Outline each blood parasite and name the species.
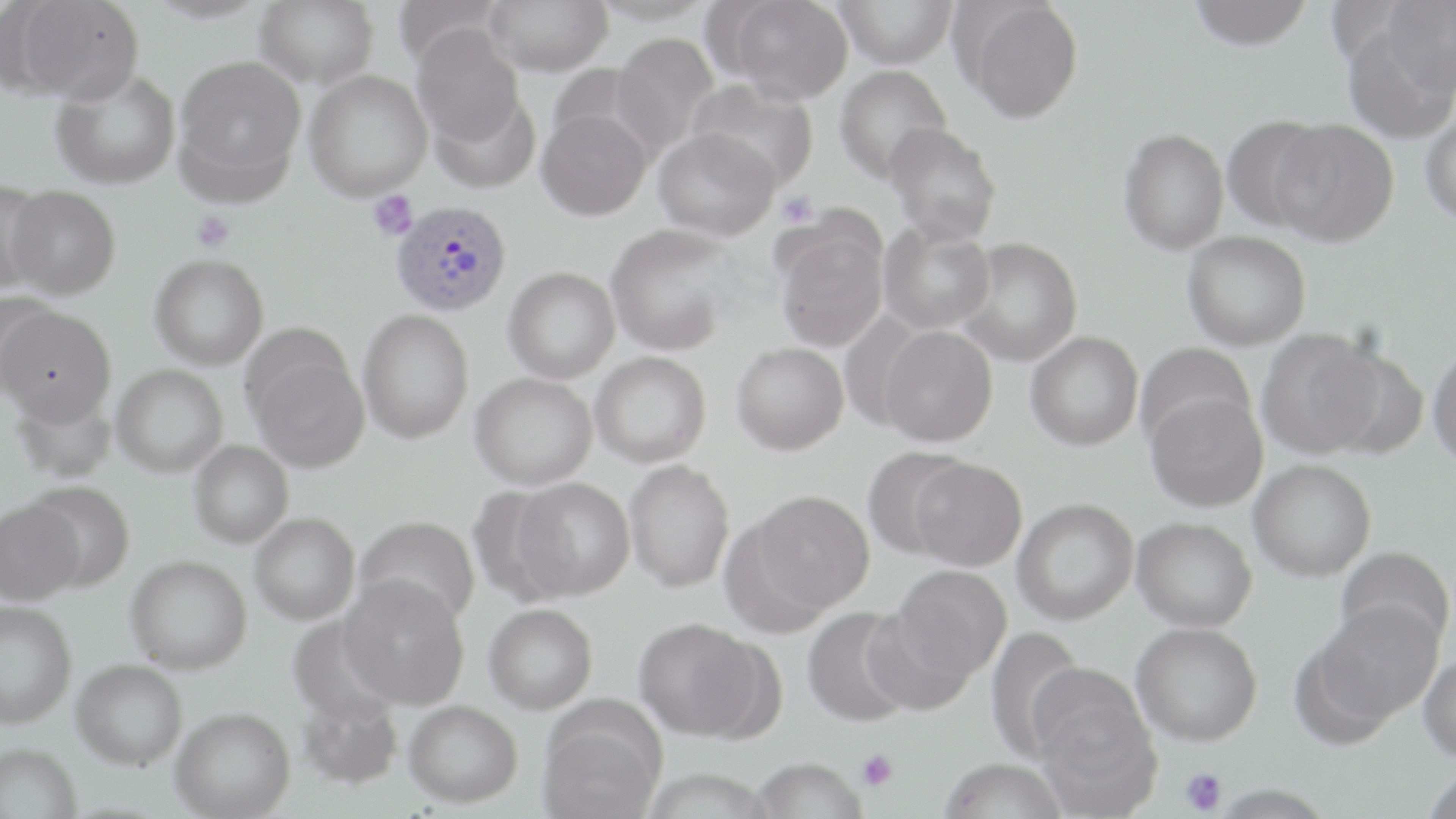
Approximate bounding boxes as (x1,y1)-(x2,y2) corner pairs in pixels.
Plasmodium vivax-infected red blood cells: (390,199)-(512,317).
No Plasmodium falciparum, Plasmodium ovale, Plasmodium malariae, Babesia divergens, or Trypanosoma brucei observed.

slide-level diagnosis = Plasmodium vivax
stain = May-Grünwald-Giemsa
preparation = thin blood smear
modality = light microscopy
uninfected red blood cell locations = approximate bounding boxes as (x1,y1)-(x2,y2) corner pairs in pixels: (11,0)-(144,103), (255,0)-(379,90), (485,0)-(613,76), (589,0)-(715,26), (725,0)-(853,104), (1187,0)-(1315,50), (1379,0)-(1456,102), (832,1)-(958,69), (961,2)-(1084,123), (411,25)-(526,148), (1342,26)-(1454,145), (611,32)-(719,156), (174,54)-(306,192), (834,64)-(952,184), (50,68)-(181,190), (303,68)-(432,201), (687,79)-(819,191), (425,90)-(539,194), (537,109)-(651,221), (1420,109)-(1456,225), (1220,115)-(1331,233), (1269,119)-(1399,246), (884,123)-(1002,245), (653,128)-(780,242), (1118,128)-(1229,255), (0,178)-(53,295), (6,184)-(121,299), (878,221)-(996,334), (605,224)-(738,356), (775,229)-(887,353), (1183,231)-(1311,350), (956,238)-(1083,366), (149,253)-(269,370), (503,266)-(620,383), (0,289)-(59,393), (0,305)-(115,425), (358,308)-(473,444), (879,325)-(998,447), (1256,330)-(1383,460), (1025,331)-(1143,451), (731,342)-(848,455), (1135,343)-(1255,451), (1428,344)-(1456,470), (1316,345)-(1430,459), (247,346)-(369,473), (590,351)-(711,468), (111,364)-(228,477), (470,372)-(597,491), (1145,392)-(1268,512), (188,440)-(293,548), (862,446)-(972,559), (909,457)-(1028,571), (1248,458)-(1376,582), (624,459)-(735,592), (513,478)-(635,600), (24,481)-(135,592), (752,489)-(874,612), (1013,498)-(1139,625), (0,499)-(85,606), (249,512)-(360,625), (354,515)-(480,628), (1132,516)-(1257,632), (1335,546)-(1455,652), (125,554)-(252,674), (892,564)-(1012,680), (339,575)-(470,709), (1311,599)-(1445,728), (0,600)-(78,728), (484,603)-(597,714), (801,607)-(917,727), (861,607)-(976,716), (633,618)-(765,740), (1131,622)-(1262,746), (982,625)-(1087,761), (1418,653)-(1456,763), (71,658)-(187,770), (296,693)-(403,791), (1031,694)-(1162,819), (403,700)-(523,807), (170,706)-(295,818), (538,717)-(664,819), (0,742)-(83,819), (751,757)-(867,819), (938,758)-(1068,819), (1420,765)-(1456,819), (640,768)-(777,818)
platelet locations = approximate bounding boxes as (x1,y1)-(x2,y2) corner pairs in pixels: (368,190)-(418,241), (777,191)-(819,227), (191,211)-(235,253), (857,750)-(897,791), (1180,767)-(1228,815)
magnification = 1000x
field of view = one of a larger specimen
image size = 1456×819 pixels